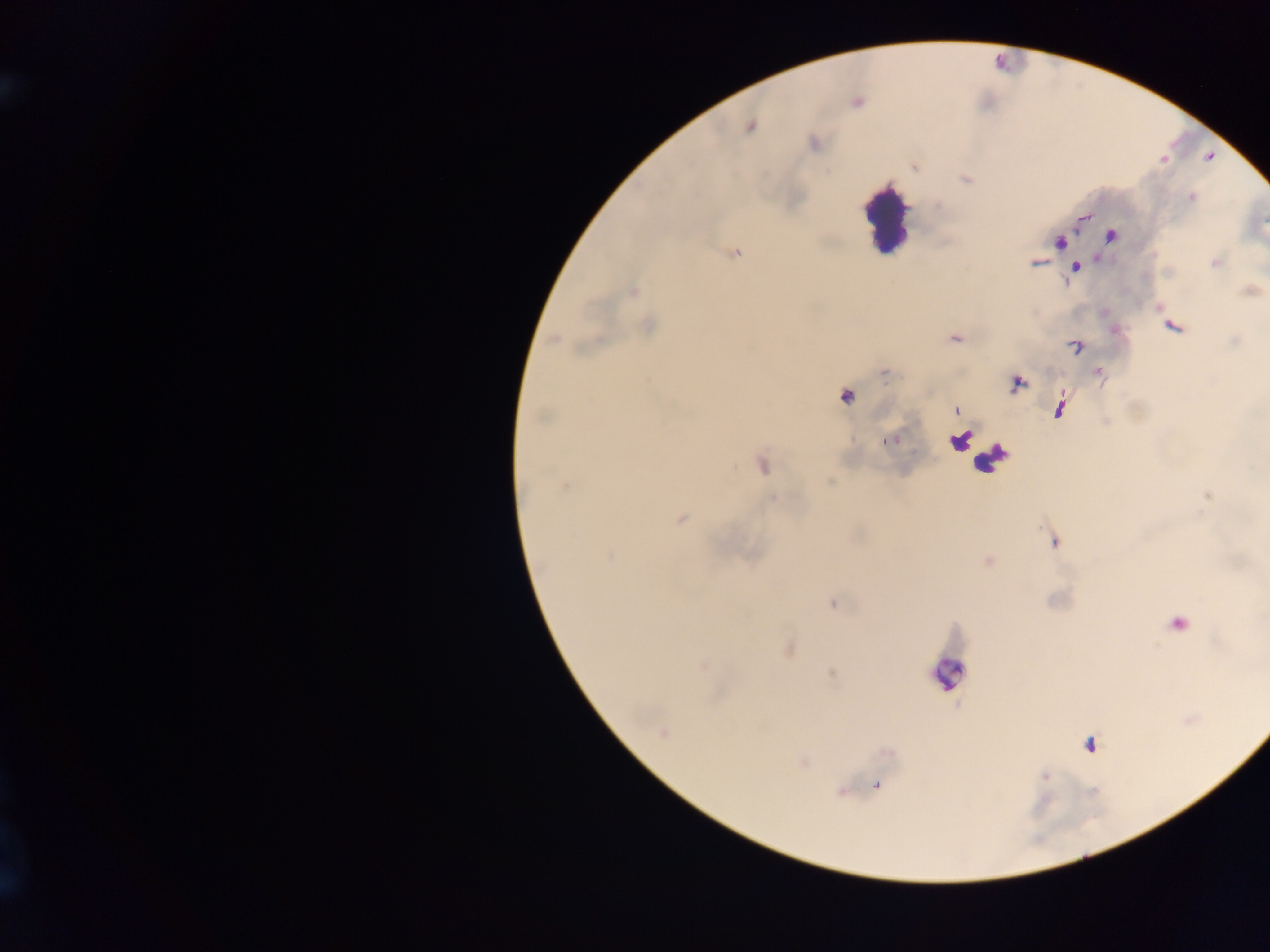

{
  "image_size": "1270×952 pixels",
  "country": "Ghana",
  "malaria_parasite_locations": "approximate centers as (x, y) in pixels: (856, 102), (749, 126), (813, 143), (915, 166), (966, 179), (1191, 197), (1082, 216), (1111, 235), (1058, 241), (734, 252), (1035, 262), (1216, 262), (1075, 267), (1250, 290), (633, 291), (648, 326), (1172, 326), (954, 338), (554, 339), (1074, 345), (884, 372), (1098, 372), (1016, 382), (845, 395), (1060, 407), (955, 409), (891, 439), (761, 464), (564, 486), (1208, 496), (772, 497), (679, 518), (1053, 541), (610, 557), (987, 561), (832, 603), (1176, 623), (788, 649), (830, 673), (662, 732), (1090, 744), (803, 762), (1044, 776), (875, 784), (840, 790)",
  "leukocyte_locations": "approximate centers as (x, y) in pixels: (1007, 61), (885, 219), (965, 444), (991, 457), (948, 672)",
  "field_of_view": "single",
  "preparation": "thick blood smear",
  "capture": "mobile-phone photograph through a microscope"
}